Give a bounding box for every trophozoite.
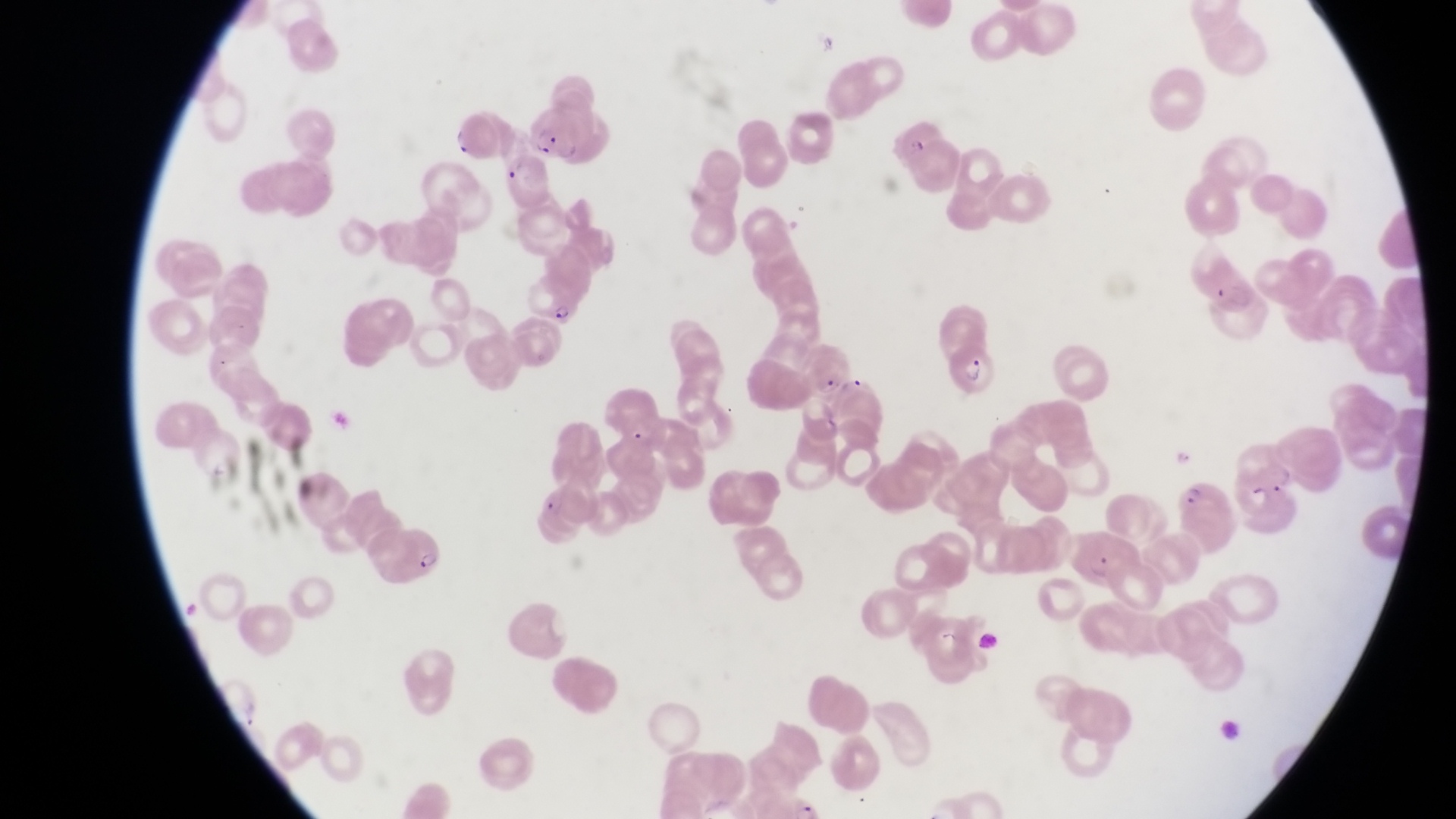

Approximate bounding boxes as (left, top, right, bottom) in pixels.
Trophozoites: (549, 296, 582, 325), (1168, 441, 1198, 473).

parasitised red blood cell locations = approximate bounding boxes as (left, top, right, bottom) in pixels: (529, 105, 578, 164), (447, 106, 502, 169), (497, 158, 553, 208), (1186, 245, 1268, 338), (944, 340, 994, 399), (802, 344, 855, 403), (1178, 482, 1234, 551), (370, 521, 447, 588), (1073, 526, 1140, 586)
country = Uganda
capture = smartphone photograph through the eyepiece of an Olympus CX-23 microscope
preparation = thin blood smear
image size = 1456×819 pixels
field of view = single
magnification = 1000x
artifact (platelet-like body, stain precipitate, or debris) locations = approximate bounding boxes as (left, top, right, bottom) in pixels: (937, 626, 970, 652)